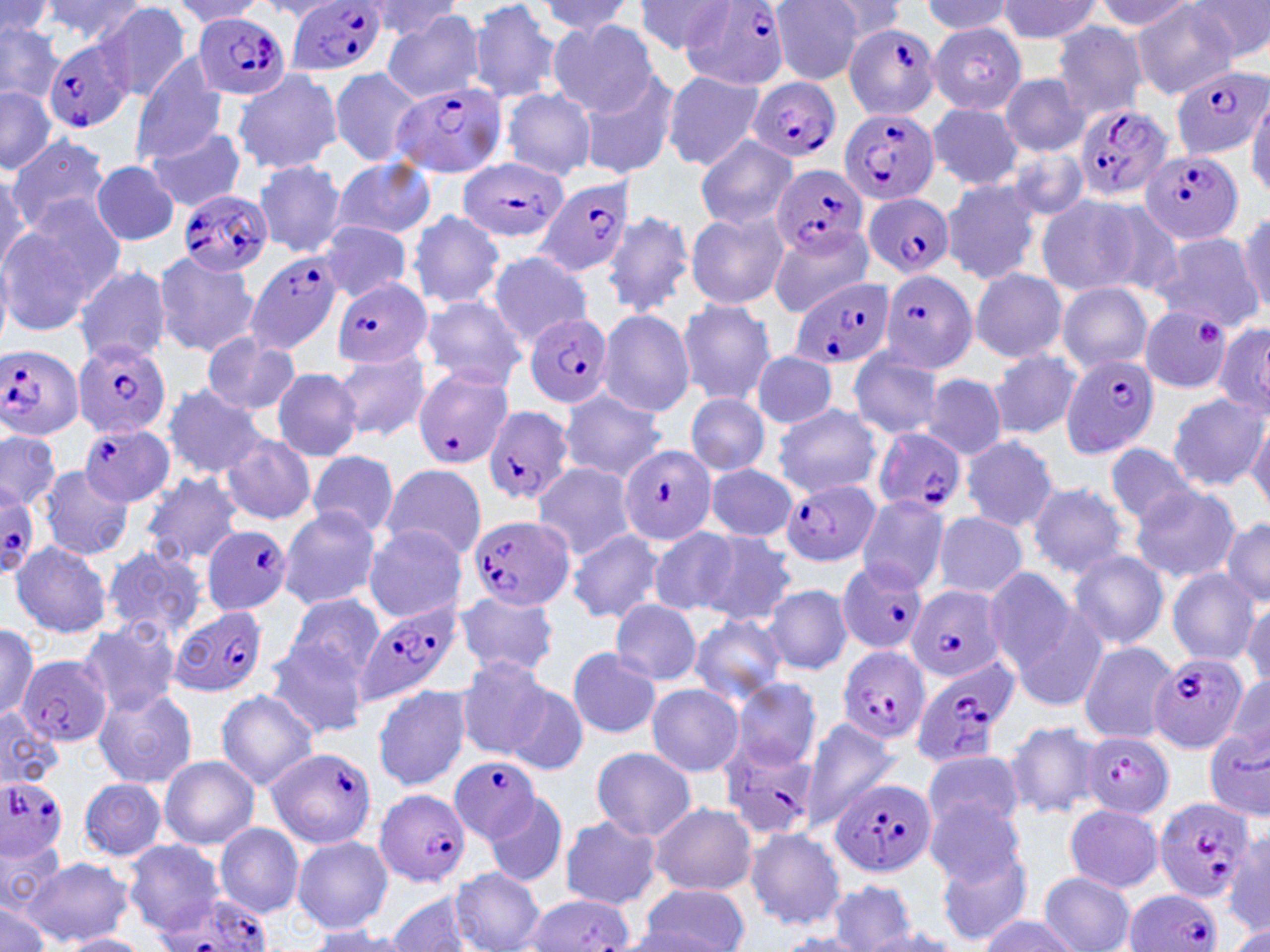
Approximate bounding boxes as [x1, y1, x2, y2] in pixels. Plasmodium falciparum-infected red blood cell locations: [287, 1, 388, 79], [681, 1, 792, 91], [197, 12, 291, 101], [844, 23, 941, 120], [45, 38, 136, 133], [1167, 65, 1270, 163], [746, 77, 839, 163], [394, 81, 508, 180], [1072, 104, 1174, 203], [837, 109, 939, 206], [1140, 148, 1242, 245], [457, 157, 570, 243], [770, 162, 868, 258], [532, 176, 638, 279], [180, 188, 274, 276], [864, 192, 956, 278], [246, 252, 344, 355], [880, 270, 978, 374], [789, 275, 894, 370], [333, 277, 434, 369], [524, 314, 612, 407], [73, 338, 171, 440], [0, 345, 84, 439], [1060, 354, 1161, 458], [413, 366, 512, 469], [481, 405, 576, 507], [78, 423, 175, 507], [873, 428, 965, 516], [617, 445, 718, 549], [782, 477, 882, 568], [1, 486, 41, 572], [467, 514, 571, 613], [201, 525, 292, 615], [837, 560, 929, 654], [906, 586, 1006, 683], [355, 603, 461, 706], [169, 605, 266, 696], [836, 647, 930, 746], [1149, 651, 1248, 755], [17, 657, 111, 746], [907, 657, 1019, 770], [1080, 732, 1173, 818], [720, 743, 818, 842], [266, 747, 377, 848], [450, 757, 543, 845], [0, 776, 69, 860], [830, 778, 933, 879], [374, 788, 471, 886], [1151, 796, 1257, 903], [1125, 890, 1222, 952], [151, 892, 274, 952]. Platelet locations: [1197, 317, 1228, 348]. Uninfected red blood cell locations: [40, 0, 149, 46], [468, 0, 564, 105], [1089, 0, 1195, 34], [1131, 0, 1241, 100], [1185, 0, 1270, 63], [169, 1, 267, 28], [533, 1, 636, 38], [770, 1, 867, 85], [815, 1, 908, 41], [920, 1, 1017, 38], [997, 1, 1104, 43], [0, 2, 56, 42], [632, 2, 735, 55], [90, 3, 192, 101], [362, 3, 462, 41], [382, 9, 486, 104], [548, 20, 660, 115], [0, 21, 67, 106], [928, 22, 1026, 114], [1051, 22, 1148, 119], [130, 57, 228, 165], [329, 67, 422, 166], [661, 69, 765, 170], [233, 70, 344, 174], [578, 71, 680, 180], [1000, 73, 1089, 157], [0, 88, 54, 174], [500, 88, 597, 180], [1247, 95, 1270, 196], [927, 102, 1023, 189], [143, 126, 247, 213], [6, 133, 110, 233], [694, 136, 798, 231], [1004, 145, 1091, 224], [331, 158, 437, 240], [91, 160, 180, 247], [253, 160, 346, 257], [0, 168, 29, 277], [940, 177, 1044, 286], [1035, 192, 1160, 299], [407, 210, 505, 310], [684, 210, 789, 310], [602, 211, 694, 318], [0, 212, 116, 336], [1235, 212, 1270, 316], [318, 222, 413, 301], [766, 223, 872, 318], [1150, 232, 1263, 329], [153, 250, 260, 357], [488, 250, 594, 347], [71, 263, 171, 365], [969, 268, 1068, 363], [1056, 282, 1154, 373], [415, 294, 529, 390], [675, 297, 775, 407], [1139, 306, 1236, 394], [596, 308, 696, 417], [1212, 321, 1270, 420], [199, 333, 300, 416], [332, 347, 432, 442], [847, 348, 946, 440], [987, 348, 1083, 439], [751, 349, 839, 429], [271, 367, 364, 461], [922, 374, 1008, 459], [163, 384, 266, 479], [558, 389, 667, 482], [1167, 392, 1265, 490], [687, 393, 768, 476], [772, 404, 883, 498], [1248, 416, 1270, 514], [0, 428, 60, 511], [960, 435, 1060, 533], [219, 436, 316, 525], [1105, 441, 1200, 529], [306, 450, 399, 538], [531, 462, 638, 560], [379, 464, 487, 562], [704, 464, 798, 542], [38, 466, 133, 561], [139, 471, 245, 568], [1027, 480, 1131, 580], [1128, 484, 1240, 582], [855, 494, 951, 595], [277, 507, 381, 610], [931, 511, 1027, 599], [1220, 516, 1270, 607], [363, 524, 469, 622], [648, 527, 739, 617], [565, 529, 666, 624], [697, 531, 798, 628], [9, 540, 112, 638], [101, 544, 208, 642], [1067, 550, 1169, 649], [981, 565, 1082, 679], [1167, 569, 1261, 666], [763, 584, 853, 675], [737, 586, 843, 731], [452, 590, 560, 678], [284, 593, 384, 685], [1005, 596, 1110, 713], [1243, 596, 1270, 691], [611, 600, 703, 685], [687, 614, 788, 707], [76, 619, 184, 716], [0, 624, 41, 722], [263, 641, 369, 738], [1077, 641, 1179, 744], [565, 649, 662, 739], [454, 656, 551, 759], [1220, 674, 1270, 765], [731, 678, 822, 770], [502, 681, 590, 777], [645, 684, 744, 777], [372, 685, 471, 790], [93, 686, 196, 787], [216, 689, 320, 790], [0, 707, 64, 789], [799, 717, 899, 830], [1002, 721, 1106, 819], [589, 747, 697, 839], [922, 749, 1023, 839], [159, 755, 260, 849], [78, 777, 166, 860], [487, 792, 567, 886], [923, 795, 1028, 889], [648, 801, 756, 896], [1062, 803, 1164, 893], [558, 817, 663, 910], [215, 823, 304, 916], [745, 826, 846, 930], [1224, 833, 1269, 935], [292, 836, 394, 932], [0, 837, 64, 917], [123, 840, 225, 932], [934, 846, 1035, 946], [22, 857, 133, 945], [449, 868, 545, 952], [1038, 871, 1135, 952], [828, 879, 915, 950], [638, 882, 749, 952], [382, 892, 476, 952], [525, 894, 633, 951], [0, 897, 54, 952], [977, 915, 1079, 952], [1227, 924, 1270, 952], [303, 926, 421, 951], [858, 930, 961, 951], [58, 933, 151, 952], [778, 933, 872, 952]. Slide-level diagnosis: Plasmodium falciparum. May-Grünwald-Giemsa-stained preparation. One field of a larger specimen. Thin blood film. Image is 1270×952 pixels. 1000x magnification. Light microscopy.